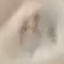
Result: no malaria parasites seen. Giemsa-stained preparation. Automatically extracted cell patch, resized to 64 × 64 pixels. Thin blood smear. Photographed with a smartphone camera at the microscope eyepiece.